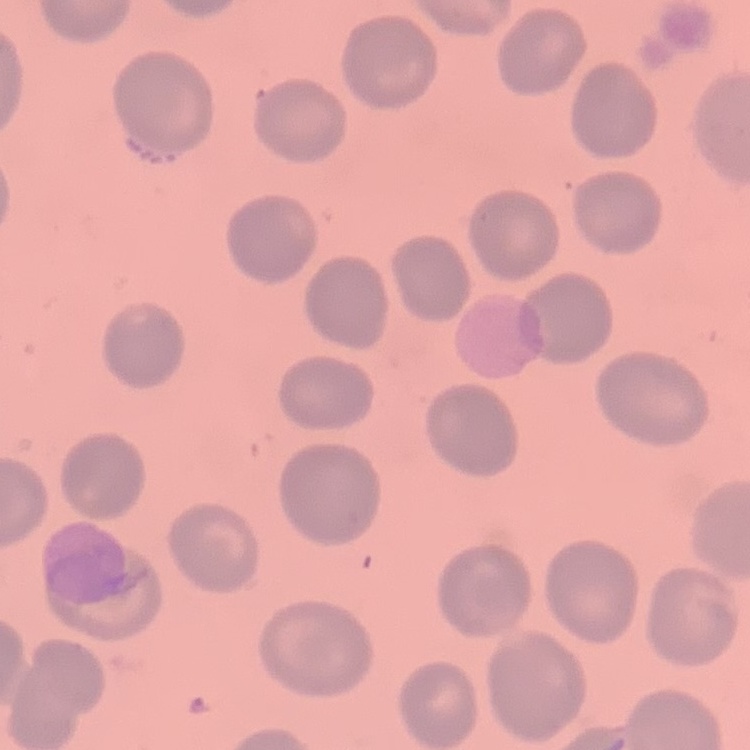

Summary:
  - Erythrocyte morphology: no rouleaux formation
  - Preparation: thin peripheral smear
  - Stain: Field's or Giemsa
  - Image type: one tile cut from a larger photomicrograph